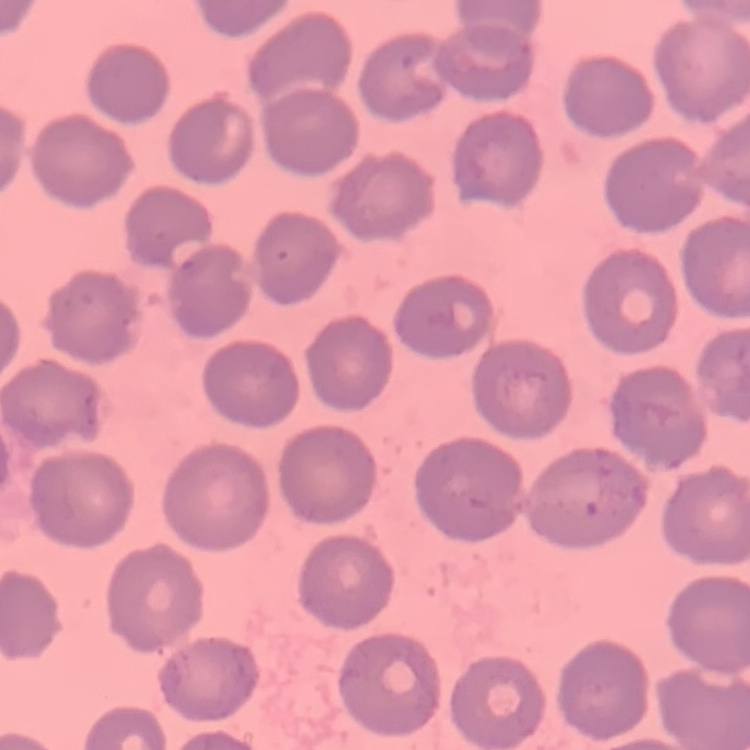

Summary:
  - Erythrocyte morphology: no rouleaux formation
  - Stain: Field's or Giemsa
  - Preparation: thin peripheral smear
  - Image type: one tile cut from a larger photomicrograph